Name the cell type shown.
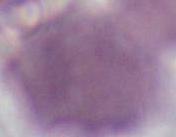
An erythrocyte.

magnification = 1000x
modality = photomicrograph